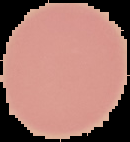

preparation = thin blood film
image size = 130×142 pixels
image type = cell region segmented out of the field of view; surrounding area masked to black
malaria status = uninfected